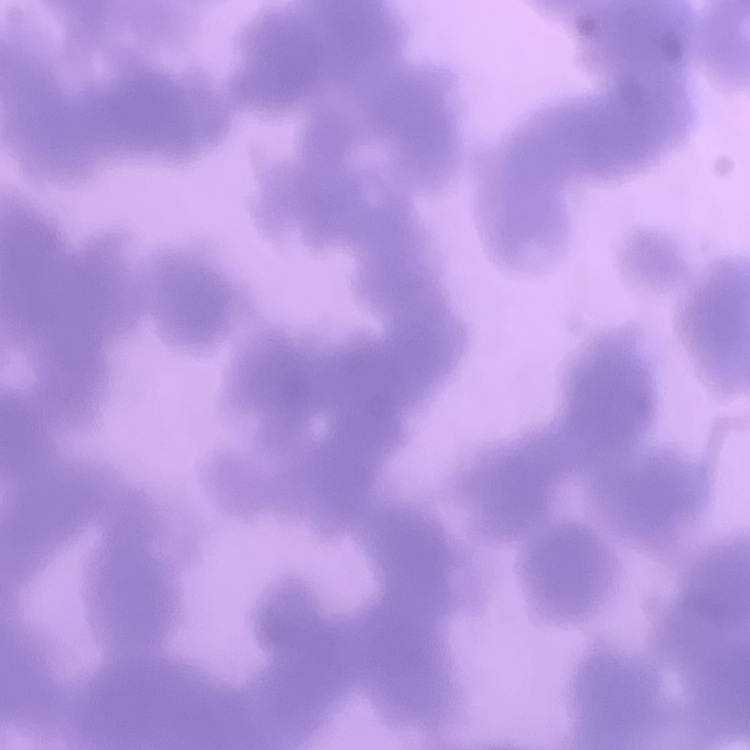 The erythrocytes show rouleaux formation. Stained with either Field's or Giemsa. Square crop of a larger photomicrograph. Thin peripheral smear.